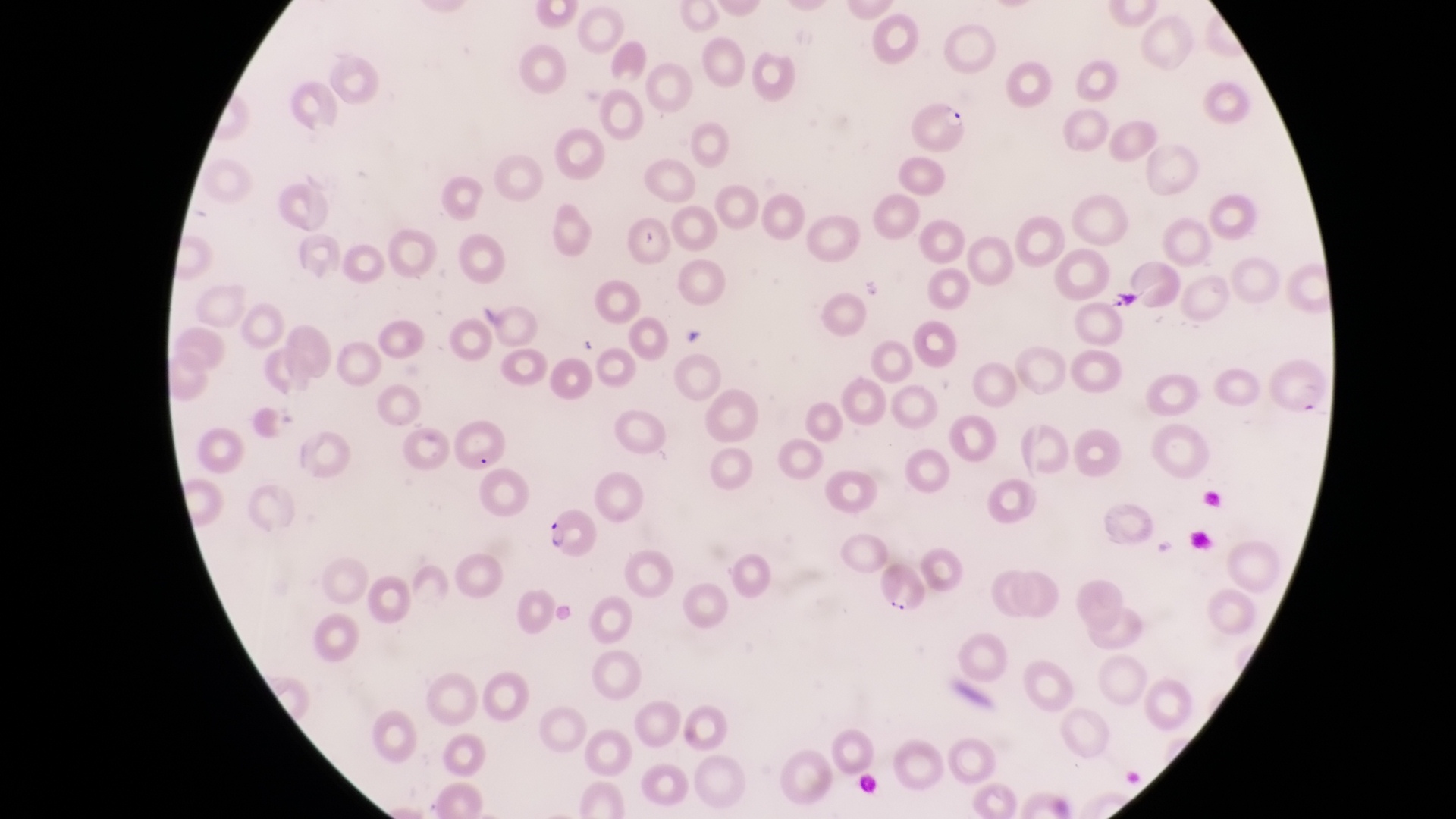
Approximate bounding boxes as [left, top, right, bottom] in pixels.
Summary:
  - Artifact (platelet-like body, stain precipitate, or debris) locations: [634, 227, 666, 256]
  - Parasitised red blood cell locations: [911, 95, 967, 158], [542, 508, 597, 564]
  - Preparation: thin blood smear
  - Country: Uganda
  - Magnification: 1000x
  - Capture: smartphone photograph through the eyepiece of an Olympus CX-23 microscope
  - Field of view: single
  - Image size: 1456×819 pixels